Report the malaria status of this cell.
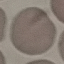

Uninfected.

image type = cell patch, automatically extracted from a larger field of view and resized to 64 × 64 pixels
capture = smartphone through the microscope eyepiece
stain = Giemsa
preparation = thin smear